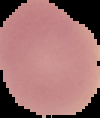

Image is 100×118 pixels. From a thin blood film. Segmented cell region on a black background. Malaria status: uninfected.